Describe the morphology of the red blood cells.
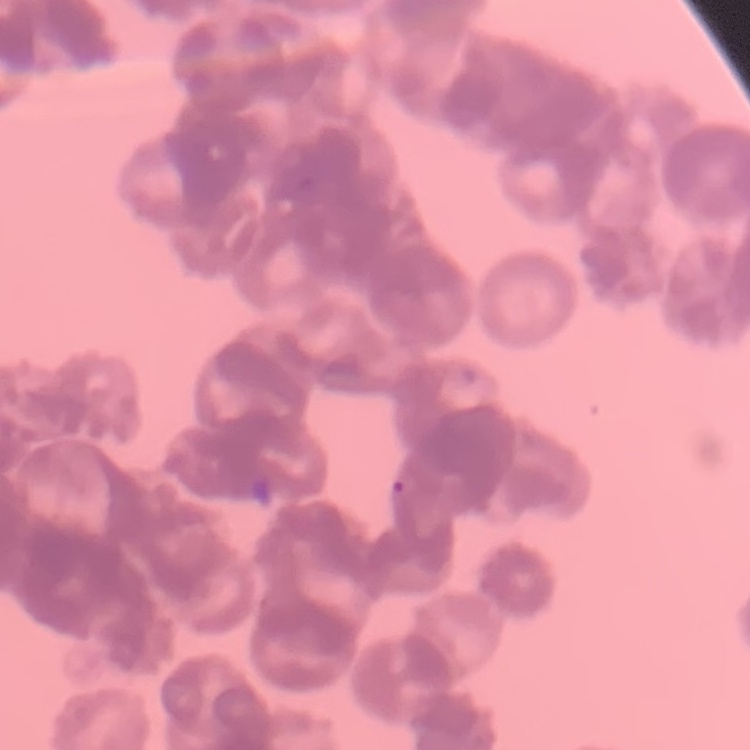

Rouleaux formation.

{
  "stain": "Field's or Giemsa",
  "preparation": "thin blood smear",
  "image_type": "one tile cut from a larger photomicrograph"
}